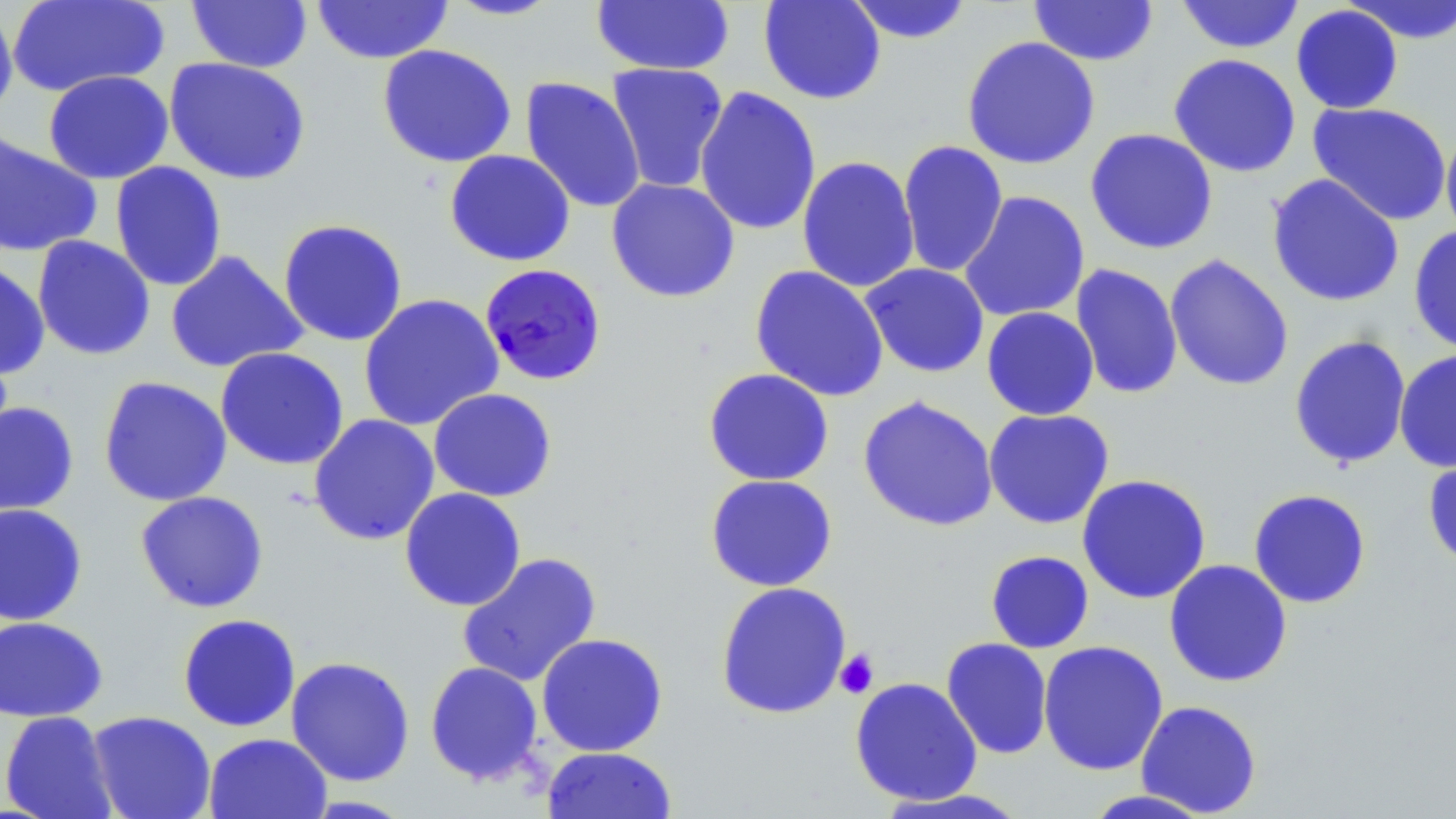 Approximate bounding boxes as named x1/y1/x2/y2 corners in pixels. Platelet locations: (x1=834, y1=648, x2=879, y2=699). Plasmodium falciparum-infected red blood cell locations: (x1=479, y1=263, x2=607, y2=387). Uninfected red blood cell locations: (x1=7, y1=0, x2=169, y2=97), (x1=443, y1=0, x2=563, y2=21), (x1=757, y1=0, x2=887, y2=105), (x1=844, y1=0, x2=974, y2=44), (x1=1028, y1=0, x2=1159, y2=66), (x1=1175, y1=0, x2=1305, y2=54), (x1=1340, y1=0, x2=1456, y2=44), (x1=186, y1=1, x2=313, y2=73), (x1=312, y1=1, x2=453, y2=64), (x1=590, y1=1, x2=735, y2=76), (x1=0, y1=2, x2=18, y2=124), (x1=1290, y1=4, x2=1404, y2=114), (x1=961, y1=35, x2=1101, y2=170), (x1=377, y1=44, x2=517, y2=168), (x1=1168, y1=53, x2=1301, y2=178), (x1=163, y1=56, x2=312, y2=185), (x1=606, y1=62, x2=729, y2=194), (x1=43, y1=70, x2=174, y2=184), (x1=520, y1=76, x2=646, y2=214), (x1=694, y1=86, x2=822, y2=236), (x1=1307, y1=102, x2=1452, y2=226), (x1=1440, y1=126, x2=1456, y2=243), (x1=1085, y1=128, x2=1219, y2=255), (x1=0, y1=131, x2=102, y2=257), (x1=897, y1=140, x2=1009, y2=278), (x1=444, y1=149, x2=575, y2=267), (x1=796, y1=155, x2=920, y2=293), (x1=110, y1=161, x2=227, y2=292), (x1=1266, y1=174, x2=1404, y2=308), (x1=606, y1=177, x2=740, y2=303), (x1=958, y1=190, x2=1090, y2=323), (x1=278, y1=218, x2=408, y2=347), (x1=1408, y1=225, x2=1456, y2=355), (x1=32, y1=235, x2=156, y2=361), (x1=165, y1=249, x2=308, y2=374), (x1=1164, y1=253, x2=1294, y2=392), (x1=0, y1=257, x2=50, y2=381), (x1=860, y1=263, x2=990, y2=378), (x1=1070, y1=264, x2=1184, y2=400), (x1=750, y1=265, x2=889, y2=402), (x1=359, y1=293, x2=504, y2=432), (x1=981, y1=306, x2=1099, y2=420), (x1=1288, y1=334, x2=1412, y2=470), (x1=215, y1=347, x2=349, y2=471), (x1=1394, y1=349, x2=1456, y2=473), (x1=703, y1=368, x2=834, y2=486), (x1=98, y1=376, x2=232, y2=507), (x1=428, y1=388, x2=558, y2=502), (x1=857, y1=395, x2=999, y2=532), (x1=0, y1=400, x2=79, y2=517), (x1=983, y1=408, x2=1115, y2=529), (x1=308, y1=414, x2=440, y2=546), (x1=1422, y1=446, x2=1456, y2=572), (x1=705, y1=474, x2=838, y2=592), (x1=1076, y1=474, x2=1212, y2=604), (x1=399, y1=487, x2=526, y2=611), (x1=1248, y1=488, x2=1372, y2=608), (x1=134, y1=491, x2=269, y2=613), (x1=0, y1=503, x2=88, y2=626), (x1=985, y1=550, x2=1095, y2=653), (x1=457, y1=552, x2=602, y2=688), (x1=1163, y1=559, x2=1293, y2=687), (x1=715, y1=581, x2=853, y2=720), (x1=177, y1=613, x2=301, y2=732), (x1=0, y1=616, x2=108, y2=722), (x1=535, y1=632, x2=668, y2=757), (x1=941, y1=637, x2=1054, y2=760), (x1=1038, y1=640, x2=1169, y2=776), (x1=286, y1=656, x2=415, y2=786), (x1=424, y1=661, x2=544, y2=786), (x1=850, y1=676, x2=983, y2=806), (x1=1135, y1=700, x2=1262, y2=817), (x1=1, y1=710, x2=118, y2=819), (x1=87, y1=711, x2=216, y2=819), (x1=203, y1=733, x2=332, y2=819), (x1=541, y1=746, x2=677, y2=819), (x1=875, y1=788, x2=1031, y2=818), (x1=1080, y1=789, x2=1215, y2=818). Slide-level diagnosis: Plasmodium falciparum. May-Grünwald-Giemsa stain. Optical microscopy. Image is 1456×819 pixels. Captured at 1000x magnification. Single field of view. Thin blood smear.